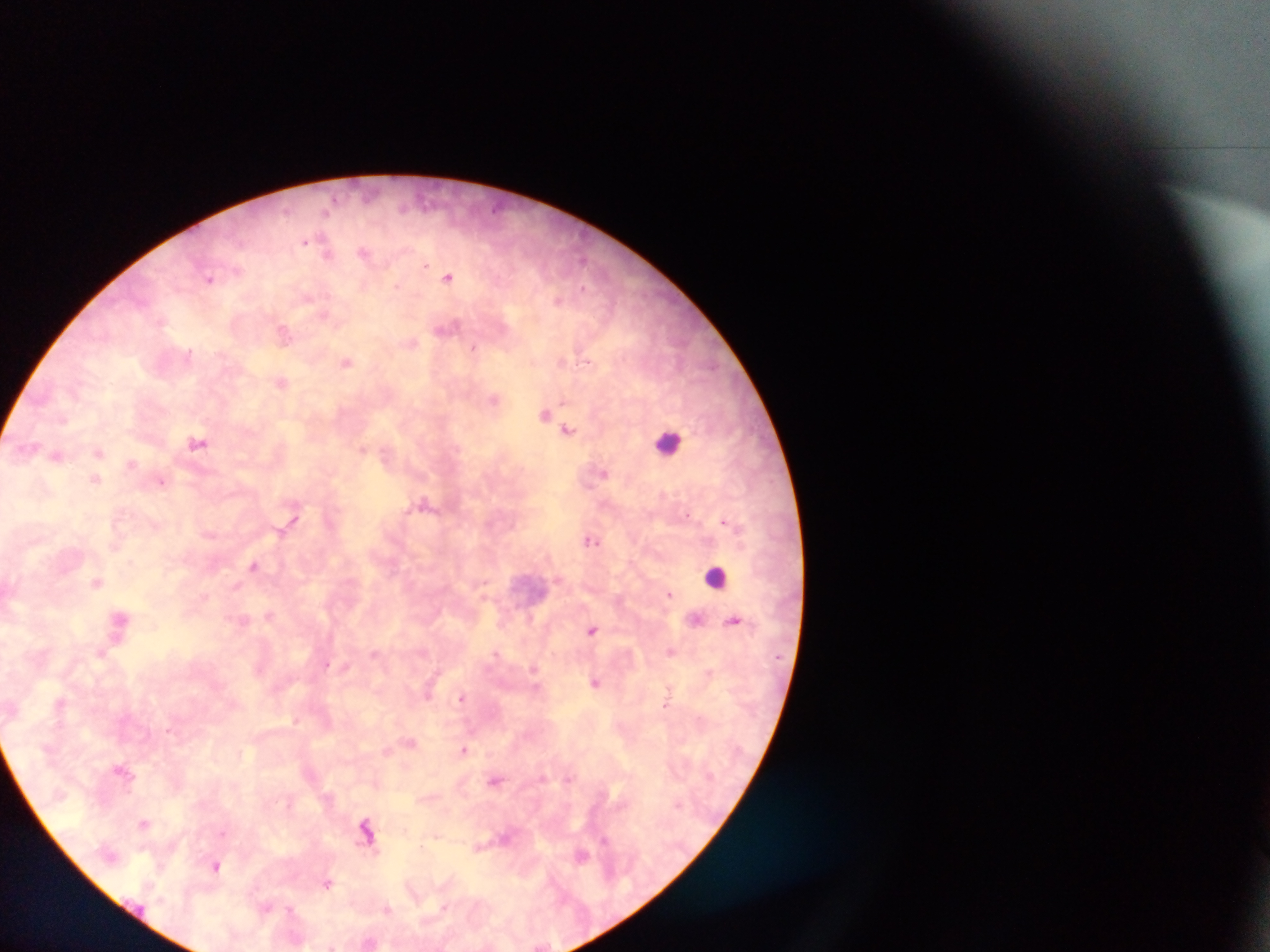 Approximate centers as x y in pixels. Leukocyte locations: 665 440; 715 580. Malaria parasite locations: 285 210; 325 212; 305 242; 363 252; 327 254; 425 265; 449 276; 210 279; 398 287; 558 301; 324 314; 449 325; 283 335; 413 341; 474 345; 189 352; 563 361; 345 362; 281 383; 564 398; 496 400; 545 414; 568 429; 198 442; 362 448; 605 472; 161 482; 589 485; 424 499; 292 518; 724 522; 593 540; 254 567; 558 581; 484 586; 671 594; 735 622; 593 629; 670 653; 375 654; 496 654; 329 665; 533 668; 709 669; 596 683; 670 685; 430 688; 463 696; 61 703; 666 704; 296 720; 169 729; 409 741; 465 750; 386 751; 124 772; 544 776; 569 780; 496 781; 376 782; 675 803; 289 804; 145 822; 407 829; 223 833; 435 836; 606 838; 483 843; 366 845; 424 845; 144 848; 583 853; 160 865; 216 865; 327 882; 267 907; 291 907; 387 910. Photographed through a microscope with a mobile-phone camera. Thick blood film. Image is 1270×952 pixels. Sample from Ghana. One field of view.